Name the blood parasite species.
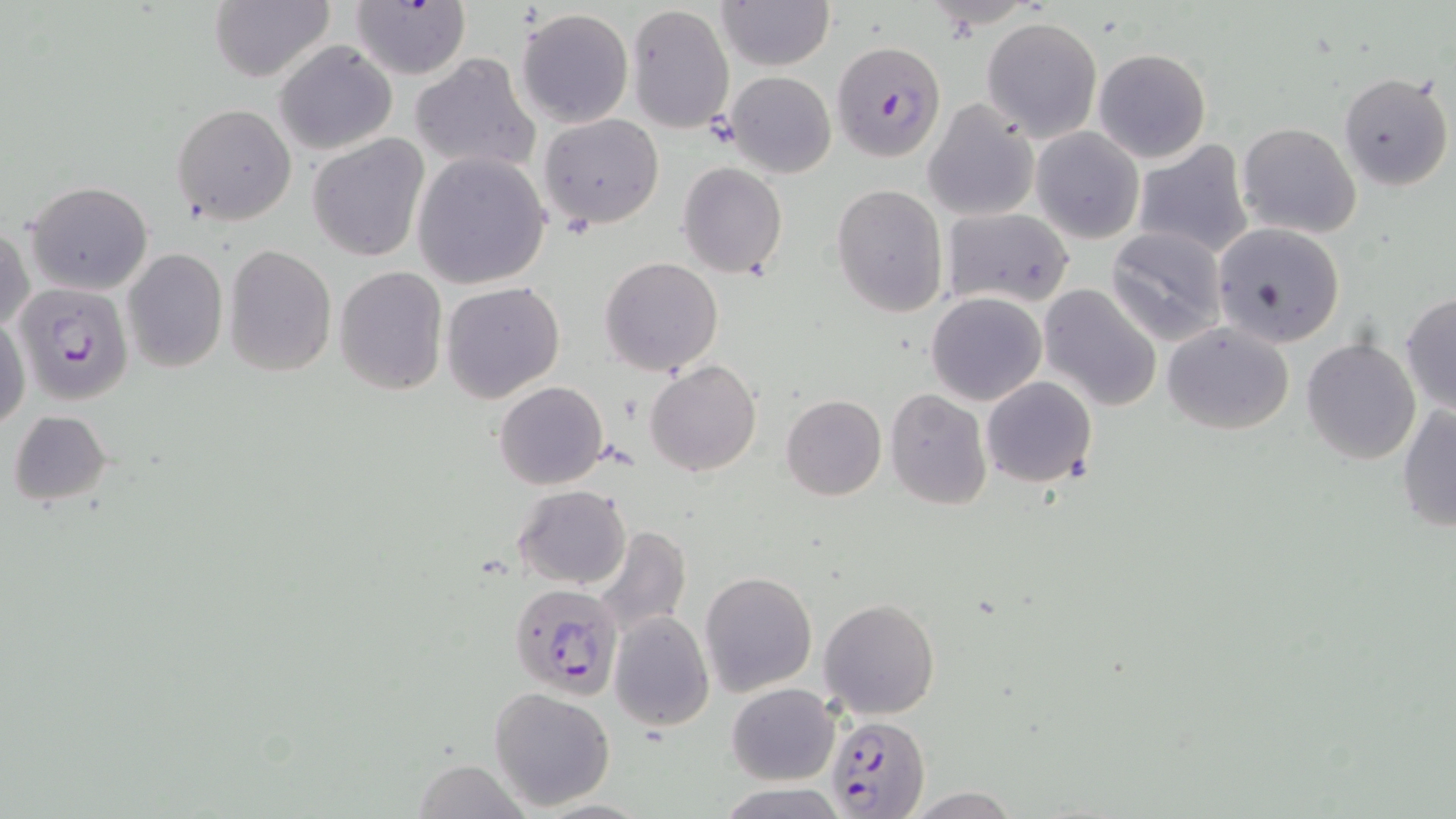

Plasmodium falciparum.

{
  "image_size": "1456×819 pixels",
  "uninfected_red_blood_cell_locations": "approximate bounding boxes as (x1, y1, x2, y2) in pixels: (210, 0, 334, 82), (351, 0, 473, 81), (718, 1, 833, 72), (626, 4, 734, 133), (516, 8, 635, 128), (981, 17, 1103, 139), (273, 40, 397, 153), (1093, 49, 1211, 163), (411, 52, 540, 175), (725, 70, 838, 178), (1336, 70, 1452, 193), (922, 99, 1040, 222), (171, 102, 296, 227), (538, 113, 664, 229), (1237, 121, 1362, 238), (1031, 126, 1144, 243), (308, 135, 429, 263), (1131, 139, 1254, 259), (413, 151, 551, 289), (678, 162, 788, 279), (25, 180, 154, 296), (832, 183, 948, 319), (941, 207, 1075, 308), (0, 220, 34, 335), (1215, 221, 1346, 346), (1106, 226, 1229, 346), (224, 244, 336, 375), (123, 248, 227, 372), (227, 257, 442, 386), (599, 257, 724, 375), (333, 267, 448, 394), (441, 280, 567, 403), (1038, 283, 1162, 412), (926, 292, 1047, 407), (1401, 292, 1455, 417), (0, 308, 29, 434), (1162, 322, 1294, 436), (1302, 336, 1420, 465), (644, 359, 762, 477), (981, 376, 1098, 488), (494, 381, 607, 491), (884, 389, 992, 510), (781, 395, 886, 501), (1395, 402, 1456, 534), (6, 409, 113, 507), (514, 484, 632, 589), (590, 525, 689, 638), (699, 571, 816, 696), (817, 598, 941, 719), (609, 613, 713, 731), (727, 683, 839, 784), (488, 686, 617, 811), (412, 760, 531, 818), (717, 784, 852, 818), (902, 787, 1025, 818)",
  "stain": "May-Grünwald-Giemsa",
  "modality": "light microscopy",
  "preparation": "thin blood smear",
  "field_of_view": "one of a larger specimen",
  "magnification": "1000x",
  "plasmodium_falciparum_infected_red_blood_cell_locations": "approximate bounding boxes as (x1, y1, x2, y2) in pixels: (832, 41, 947, 161), (24, 281, 135, 410), (508, 582, 624, 700), (826, 715, 930, 817)"
}